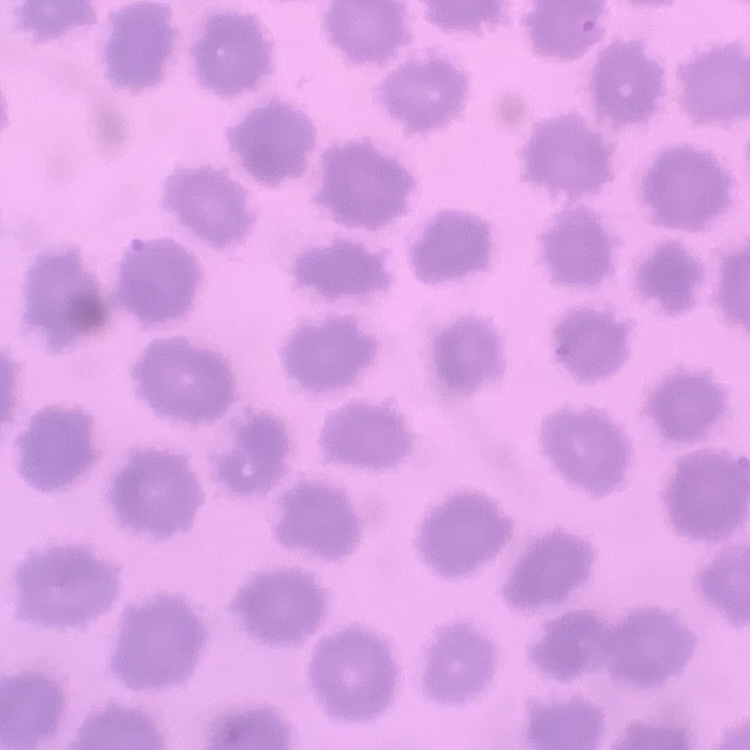
{
  "erythrocyte_morphology": "no rouleaux formation",
  "stain": "Field's or Giemsa",
  "preparation": "thin blood film",
  "image_type": "square crop of a larger photomicrograph"
}